Locate every Plasmodium parasite.
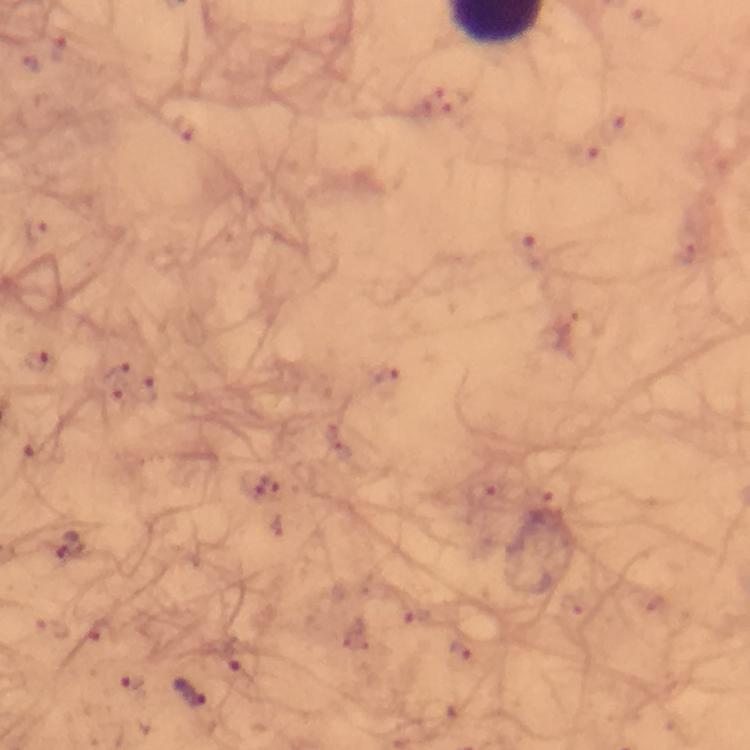

Approximate centers as {x, y} in pixels.
Plasmodium parasites: {68, 546}, {189, 691}.

Summary:
  - Image size: 750×750 pixels
  - Cropped from: one field of view
  - Preparation: thick blood film
  - Magnification: 100x
  - Context: from a malaria diagnostic workup
  - Immersion oil: applied
  - Stain: Giemsa
  - Capture: smartphone mounted on the microscope